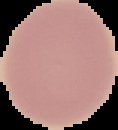
preparation = thin blood smear
image size = 118×130 pixels
image type = cell region segmented out of the field of view; surrounding area masked to black
malaria status = uninfected